Locate and identify every blood parasite.
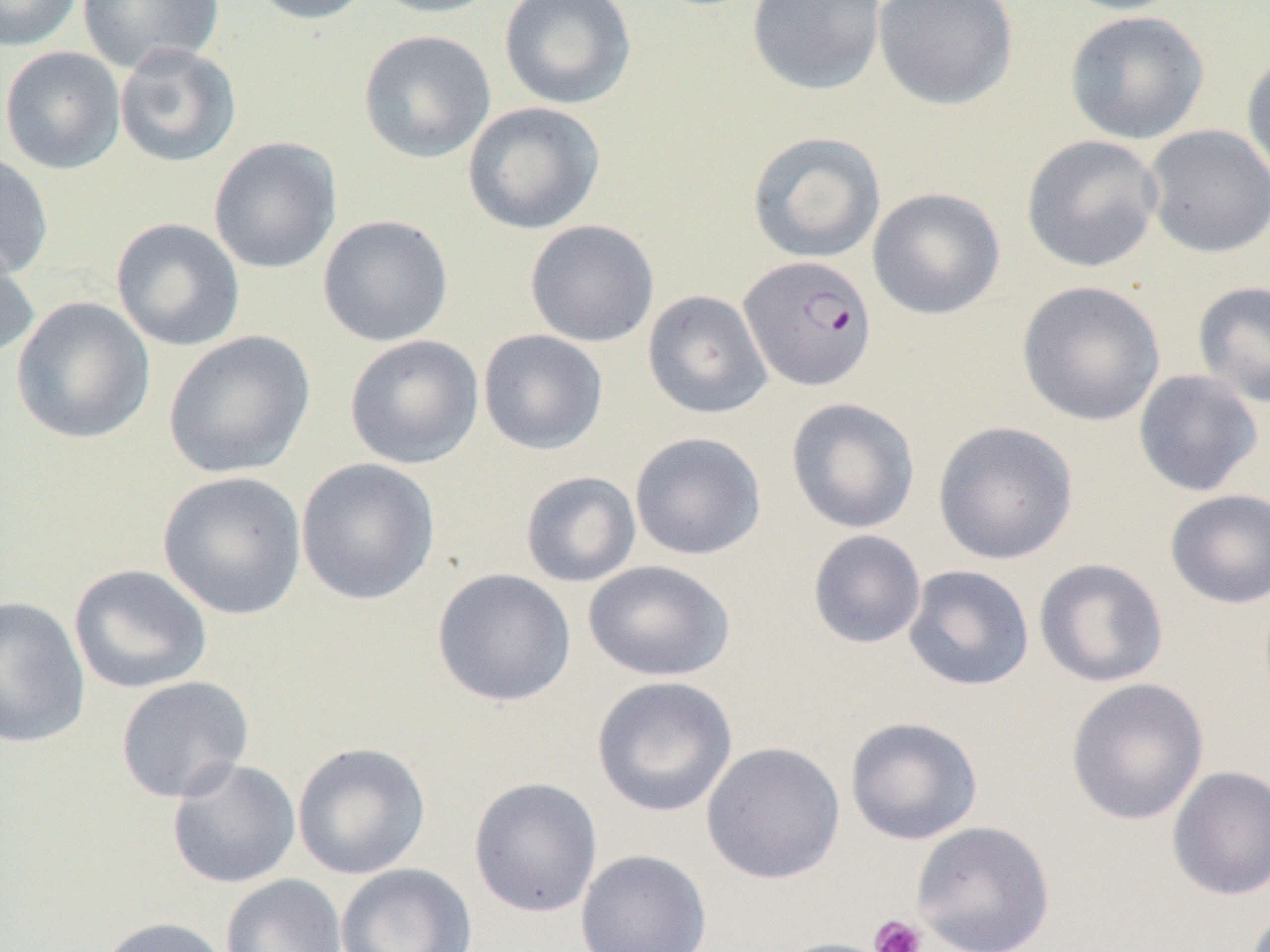

Approximate bounding boxes as (x1, y1, x2, y2) in pixels.
Plasmodium falciparum-infected red blood cells: (738, 255, 877, 391).
No Plasmodium ovale, Plasmodium malariae, Plasmodium vivax, Babesia divergens, or Trypanosoma brucei observed.

Summary:
  - Uninfected red blood cell locations: (0, 0, 82, 52), (76, 0, 224, 74), (244, 0, 377, 25), (365, 0, 507, 18), (499, 0, 637, 109), (746, 0, 886, 96), (872, 0, 1019, 110), (1055, 0, 1189, 16), (1064, 10, 1209, 144), (358, 30, 496, 163), (113, 42, 242, 169), (0, 45, 126, 175), (1241, 50, 1270, 187), (462, 101, 606, 234), (1143, 124, 1270, 258), (746, 131, 886, 264), (1021, 134, 1163, 273), (209, 136, 343, 275), (0, 151, 53, 281), (868, 188, 1006, 320), (317, 214, 454, 347), (110, 218, 245, 352), (524, 219, 659, 347), (0, 238, 39, 362), (1016, 280, 1166, 426), (1192, 280, 1270, 410), (642, 290, 772, 419), (11, 296, 156, 445), (477, 329, 609, 456), (163, 330, 315, 480), (344, 334, 484, 469), (1132, 369, 1264, 497), (785, 397, 921, 534), (932, 420, 1079, 566), (629, 431, 767, 561), (295, 457, 441, 606), (158, 471, 307, 620), (520, 471, 642, 588), (1164, 488, 1270, 609), (807, 529, 927, 649), (1034, 558, 1169, 688), (583, 560, 735, 682), (68, 564, 213, 694), (902, 564, 1035, 692), (431, 568, 577, 707), (0, 595, 91, 749), (115, 676, 254, 804), (591, 676, 738, 818), (1066, 678, 1209, 825), (845, 716, 984, 845), (292, 741, 432, 880), (701, 741, 846, 884), (166, 758, 302, 889), (1167, 766, 1270, 901), (468, 776, 603, 917), (910, 820, 1056, 952), (575, 848, 712, 952), (335, 862, 477, 952), (220, 874, 348, 952), (93, 916, 234, 952), (769, 937, 900, 952)
  - Platelet locations: (869, 914, 927, 952)
  - Slide-level diagnosis: Plasmodium falciparum
  - Image size: 1270×952 pixels
  - Modality: light microscopy
  - Magnification: 1000x
  - Preparation: thin blood film
  - Field of view: single